Classify this cell by malaria status.
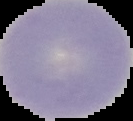
Uninfected.

Image is 133×121 pixels. From a thin blood smear. The area outside the segmented cell region is set to black.